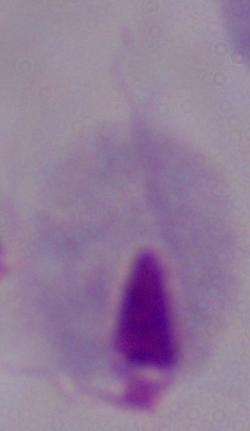
magnification = 1000x
identification = trichomonad
modality = photomicrograph